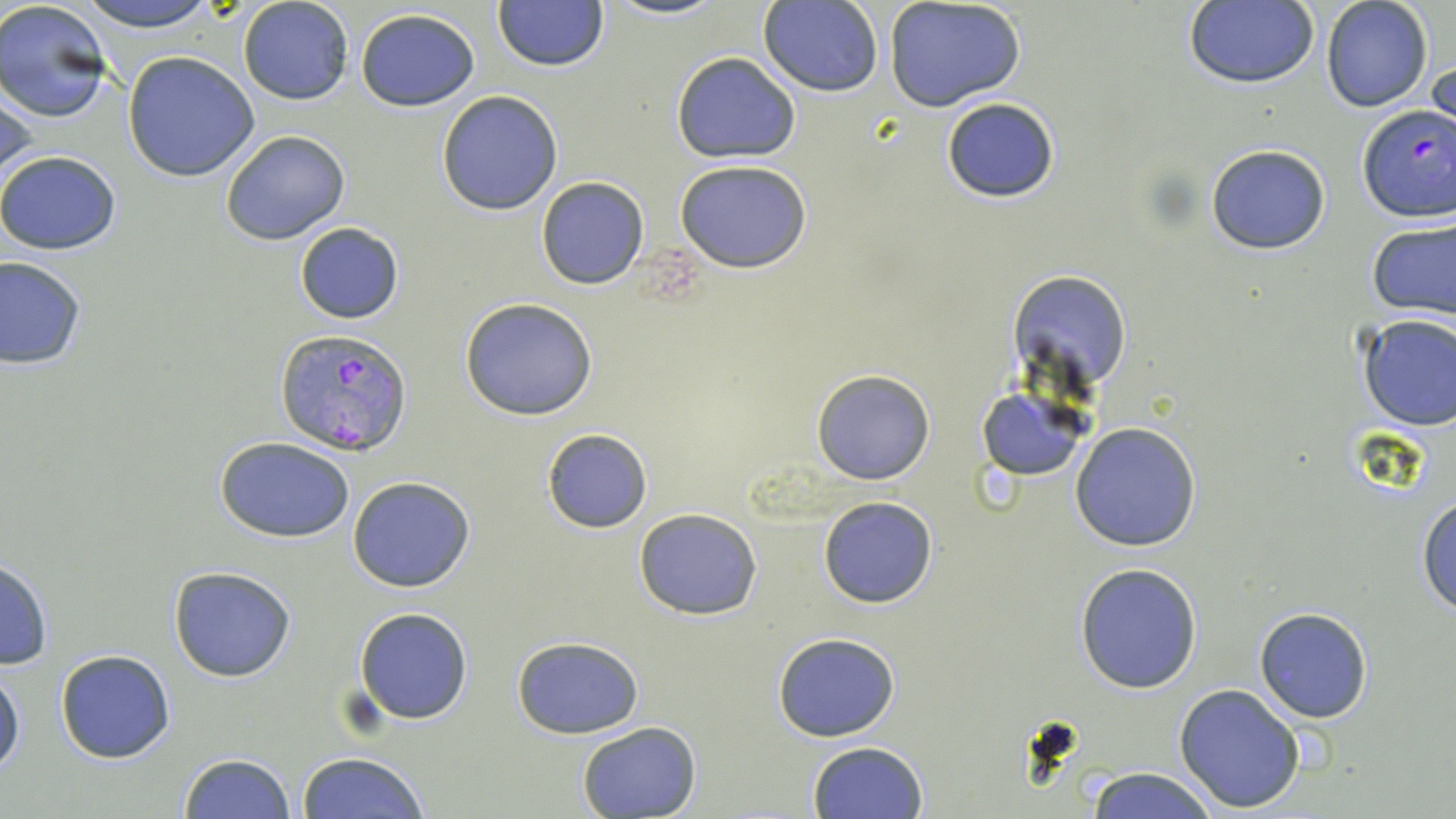

Summary:
  - Coordinate format: approximate bounding boxes as named x1/y1/x2/y2 corners in pixels
  - Plasmodium falciparum-infected red blood cell locations: (x1=1357, y1=106, x2=1455, y2=223), (x1=276, y1=329, x2=411, y2=455)
  - Uninfected red blood cell locations: (x1=71, y1=0, x2=229, y2=32), (x1=238, y1=0, x2=355, y2=106), (x1=603, y1=0, x2=729, y2=21), (x1=1320, y1=0, x2=1433, y2=113), (x1=0, y1=1, x2=115, y2=124), (x1=759, y1=1, x2=883, y2=96), (x1=883, y1=1, x2=1026, y2=112), (x1=1182, y1=1, x2=1319, y2=89), (x1=492, y1=2, x2=609, y2=73), (x1=354, y1=8, x2=482, y2=111), (x1=1428, y1=50, x2=1455, y2=151), (x1=122, y1=51, x2=261, y2=181), (x1=671, y1=51, x2=801, y2=164), (x1=1, y1=77, x2=37, y2=192), (x1=436, y1=91, x2=563, y2=215), (x1=940, y1=97, x2=1060, y2=203), (x1=220, y1=129, x2=350, y2=246), (x1=1205, y1=142, x2=1332, y2=256), (x1=0, y1=150, x2=122, y2=255), (x1=675, y1=161, x2=813, y2=274), (x1=536, y1=176, x2=649, y2=290), (x1=1366, y1=218, x2=1456, y2=323), (x1=294, y1=221, x2=404, y2=324), (x1=1, y1=255, x2=85, y2=371), (x1=1011, y1=271, x2=1131, y2=391), (x1=459, y1=298, x2=599, y2=421), (x1=1355, y1=313, x2=1456, y2=431), (x1=811, y1=369, x2=935, y2=486), (x1=976, y1=387, x2=1088, y2=481), (x1=1069, y1=422, x2=1202, y2=552), (x1=541, y1=429, x2=652, y2=532), (x1=215, y1=435, x2=356, y2=542), (x1=347, y1=476, x2=476, y2=592), (x1=1417, y1=493, x2=1456, y2=618), (x1=817, y1=496, x2=938, y2=609), (x1=634, y1=508, x2=763, y2=621), (x1=0, y1=555, x2=53, y2=671), (x1=1074, y1=563, x2=1204, y2=694), (x1=168, y1=566, x2=296, y2=681), (x1=354, y1=607, x2=473, y2=724), (x1=1254, y1=607, x2=1373, y2=723), (x1=772, y1=632, x2=902, y2=742), (x1=511, y1=635, x2=644, y2=739), (x1=54, y1=648, x2=177, y2=764), (x1=0, y1=667, x2=24, y2=779), (x1=1174, y1=682, x2=1306, y2=813), (x1=575, y1=720, x2=701, y2=819), (x1=807, y1=741, x2=928, y2=818), (x1=177, y1=752, x2=296, y2=819), (x1=296, y1=752, x2=430, y2=819), (x1=1082, y1=766, x2=1222, y2=819)
  - Slide-level diagnosis: Plasmodium falciparum
  - Image size: 1456×819 pixels
  - Stain: May-Grünwald-Giemsa
  - Magnification: 1000x
  - Preparation: thin blood film
  - Field of view: single
  - Modality: optical microscopy